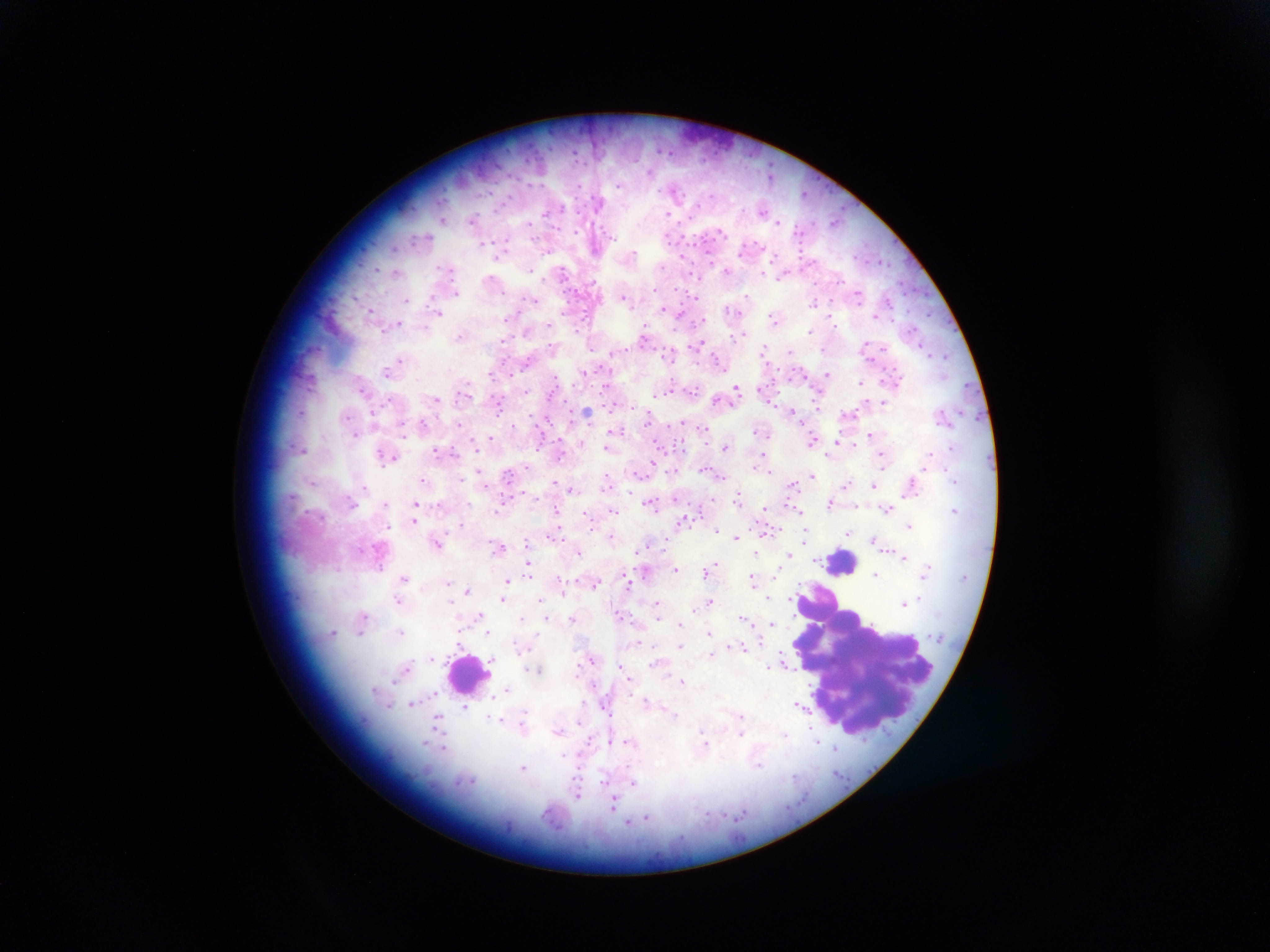

Approximate centers as x y in pixels.
Summary:
  - Malaria parasite locations: 666 152; 573 154; 770 176; 617 186; 674 191; 803 193; 600 199; 700 204; 503 206; 764 210; 546 212; 670 215; 689 218; 473 220; 837 220; 530 225; 722 231; 802 231; 575 233; 480 243; 668 244; 693 244; 392 248; 634 251; 743 251; 499 255; 855 255; 663 266; 375 269; 530 270; 727 270; 561 272; 395 273; 779 276; 490 277; 697 277; 816 281; 655 290; 455 291; 696 292; 747 294; 626 297; 408 298; 532 300; 813 304; 370 308; 662 310; 729 311; 439 313; 563 314; 927 314; 678 315; 773 319; 397 321; 506 322; 550 326; 837 328; 811 329; 646 330; 527 331; 577 331; 730 335; 744 335; 700 344; 549 345; 654 347; 626 348; 868 348; 671 349; 591 350; 928 350; 789 352; 762 354; 947 355; 400 358; 527 359; 672 362; 719 362; 827 374; 490 376; 511 376; 555 377; 805 378; 606 385; 861 385; 736 387; 361 391; 668 391; 527 392; 662 392; 696 392; 548 395; 387 399; 436 400; 566 400; 768 401; 498 403; 821 405; 793 410; 588 411; 648 411; 611 412; 302 413; 530 414; 420 419; 549 420; 682 422; 458 425; 515 425; 705 430; 757 430; 353 433; 763 433; 869 434; 403 437; 491 438; 469 440; 812 441; 836 441; 660 443; 834 446; 725 447; 301 448; 605 448; 434 450; 539 451; 454 452; 928 454; 763 456; 388 458; 884 458; 561 459; 654 465; 526 467; 708 469; 479 471; 771 472; 507 474; 813 475; 722 476; 953 476; 608 477; 423 479; 954 479; 462 481; 606 482; 309 483; 553 483; 846 483; 874 485; 792 486; 365 487; 572 488; 524 491; 293 494; 629 495; 676 497; 738 498; 712 499; 417 502; 828 504; 655 505; 497 507; 764 509; 887 510; 613 511; 556 512; 801 512; 701 514; 588 516; 416 520; 592 523; 462 524; 390 526; 908 526; 692 527; 717 527; 773 528; 805 532; 847 534; 550 535; 735 535; 874 540; 440 541; 500 547; 638 549; 757 550; 579 551; 788 555; 904 558; 819 559; 712 564; 528 567; 637 568; 675 568; 705 570; 876 573; 404 577; 753 579; 509 581; 449 582; 597 583; 630 586; 466 590; 563 590; 448 597; 918 597; 398 598; 502 598; 541 598; 709 599; 768 599; 792 599; 657 604; 902 604; 696 605; 692 610; 619 612; 476 615; 361 616; 522 618; 572 618; 546 619; 743 619; 657 621; 681 622; 772 623; 400 630; 332 631; 360 632; 488 632; 708 632; 639 641; 458 644; 655 646; 679 646; 740 647; 711 654; 432 657; 493 661; 783 665; 623 666; 767 667; 406 669; 539 670; 531 671; 577 678; 629 679; 681 681; 594 686; 506 688; 377 690; 646 701; 411 703; 386 704; 799 705; 464 706; 604 708; 524 712; 674 714; 490 718; 437 719; 558 733; 741 733; 703 738; 426 741; 608 741; 819 741; 628 742; 707 743; 445 748; 835 749; 566 757; 759 765; 524 767; 604 779; 473 781; 633 781; 577 794; 614 803; 647 817; 629 820
  - Leukocyte locations: 841 563; 868 661; 468 671
  - Country: Ghana
  - Capture: mobile-phone photograph through a microscope
  - Preparation: thick blood smear
  - Image size: 1270×952 pixels
  - Field of view: single